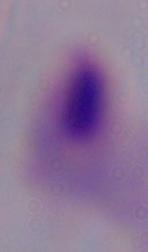
Summary:
  - Modality: micrograph
  - Identification: trichomonad
  - Magnification: 1000x